Give the position of every leukocyte visible.
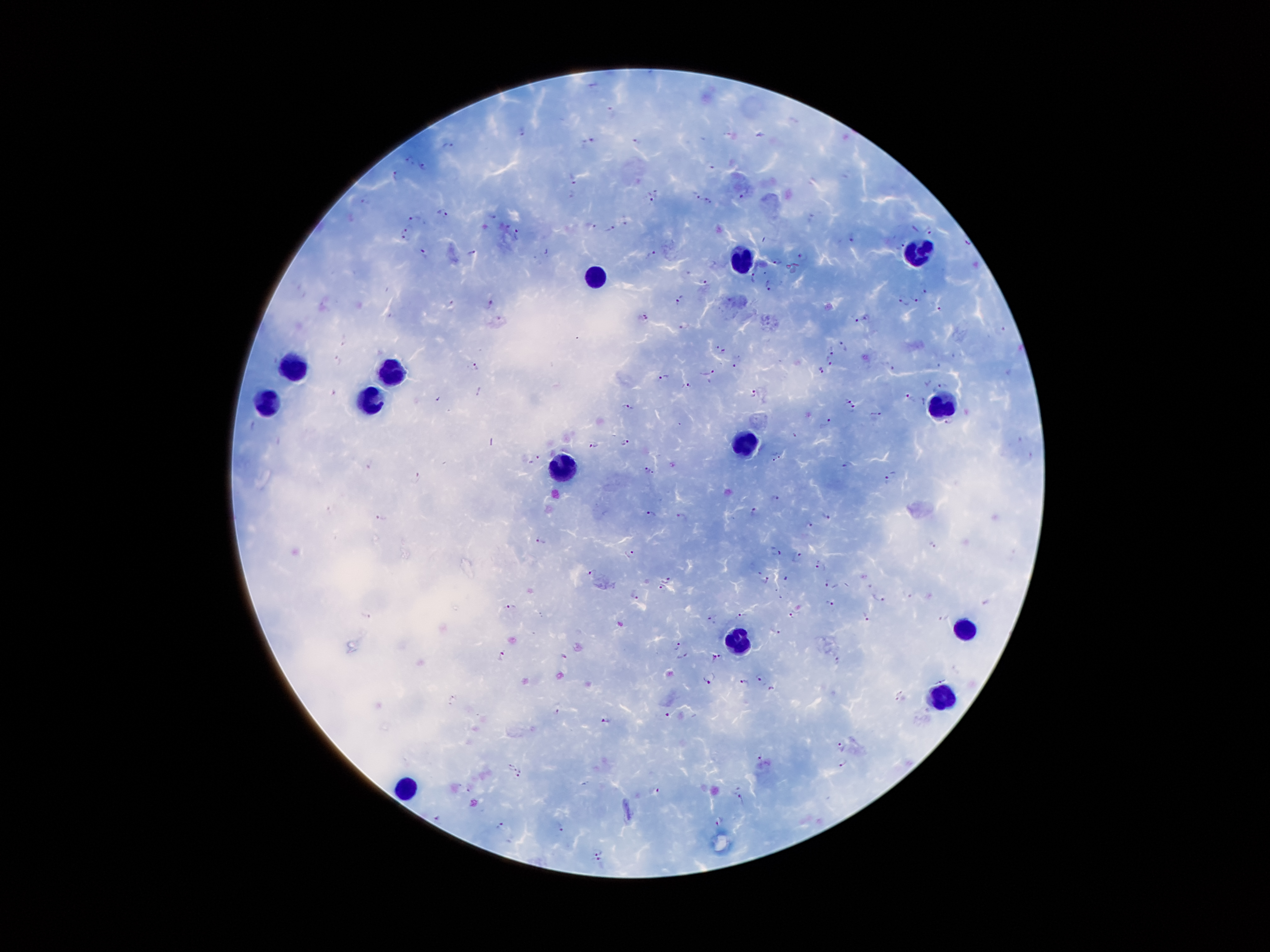
Approximate object centers, in pixels from the top-left corner.
Leukocytes: (x=921, y=253), (x=745, y=257), (x=595, y=279), (x=298, y=369), (x=397, y=371), (x=370, y=398), (x=269, y=400), (x=936, y=408), (x=742, y=444), (x=566, y=465), (x=967, y=624), (x=740, y=639), (x=947, y=699), (x=405, y=785).

Plasmodium parasite locations = (x=523, y=132), (x=587, y=140), (x=635, y=142), (x=448, y=145), (x=409, y=160), (x=712, y=164), (x=421, y=165), (x=396, y=175), (x=572, y=179), (x=571, y=194), (x=697, y=194), (x=743, y=194), (x=651, y=196), (x=364, y=199), (x=710, y=201), (x=442, y=211), (x=494, y=217), (x=626, y=218), (x=412, y=219), (x=590, y=225), (x=610, y=228), (x=408, y=229), (x=930, y=230), (x=402, y=234), (x=516, y=234), (x=853, y=236), (x=901, y=242), (x=425, y=251), (x=474, y=253), (x=653, y=255), (x=803, y=257), (x=776, y=262), (x=755, y=279), (x=704, y=283), (x=768, y=285), (x=925, y=288), (x=914, y=298), (x=680, y=299), (x=904, y=302), (x=487, y=303), (x=938, y=308), (x=644, y=317), (x=854, y=317), (x=684, y=326), (x=1002, y=329), (x=343, y=341), (x=844, y=345), (x=717, y=346), (x=724, y=352), (x=830, y=352), (x=954, y=355), (x=339, y=361), (x=828, y=364), (x=736, y=365), (x=889, y=365), (x=477, y=367), (x=819, y=370), (x=706, y=372), (x=663, y=377), (x=944, y=385), (x=687, y=387), (x=334, y=392), (x=753, y=394), (x=910, y=397), (x=849, y=400), (x=628, y=408), (x=854, y=408), (x=877, y=414), (x=829, y=423), (x=796, y=436), (x=626, y=442), (x=594, y=445), (x=779, y=454), (x=771, y=458), (x=536, y=460), (x=849, y=466), (x=646, y=469), (x=654, y=473), (x=419, y=478), (x=891, y=480), (x=774, y=497), (x=755, y=512), (x=651, y=513), (x=825, y=516), (x=382, y=517), (x=682, y=517), (x=810, y=525), (x=541, y=540), (x=932, y=545), (x=775, y=550), (x=628, y=553), (x=798, y=556), (x=821, y=566), (x=592, y=572), (x=760, y=572), (x=786, y=578), (x=667, y=580), (x=767, y=580), (x=827, y=584), (x=661, y=589), (x=634, y=594), (x=879, y=598), (x=829, y=603), (x=510, y=608), (x=743, y=615), (x=791, y=615), (x=866, y=617), (x=946, y=617), (x=712, y=619), (x=776, y=629), (x=675, y=640), (x=502, y=655), (x=686, y=657), (x=718, y=657), (x=838, y=661), (x=759, y=676), (x=710, y=679), (x=743, y=683), (x=771, y=688), (x=561, y=710), (x=669, y=717), (x=603, y=722), (x=840, y=745), (x=759, y=757), (x=843, y=762), (x=511, y=767), (x=520, y=774), (x=658, y=791), (x=742, y=799), (x=437, y=817), (x=719, y=821), (x=560, y=826), (x=499, y=827), (x=599, y=851), (x=596, y=862)
preparation = thick peripheral-blood smear
stain = Giemsa
magnification = 100x
patient malaria status = infected with Plasmodium falciparum
capture = smartphone through the microscope eyepiece
field of view = one from this slide
image size = 1270×952 pixels